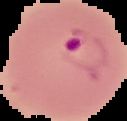
image_type: segmented cell region with the area outside set to black
result: malaria parasites detected
image_size: 127×121 pixels
preparation: thin blood film